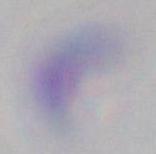
Summary:
  - Magnification: 1000x
  - Identification: Toxoplasma gondii
  - Modality: photomicrograph